Locate every Plasmodium falciparum-infected red blood cell.
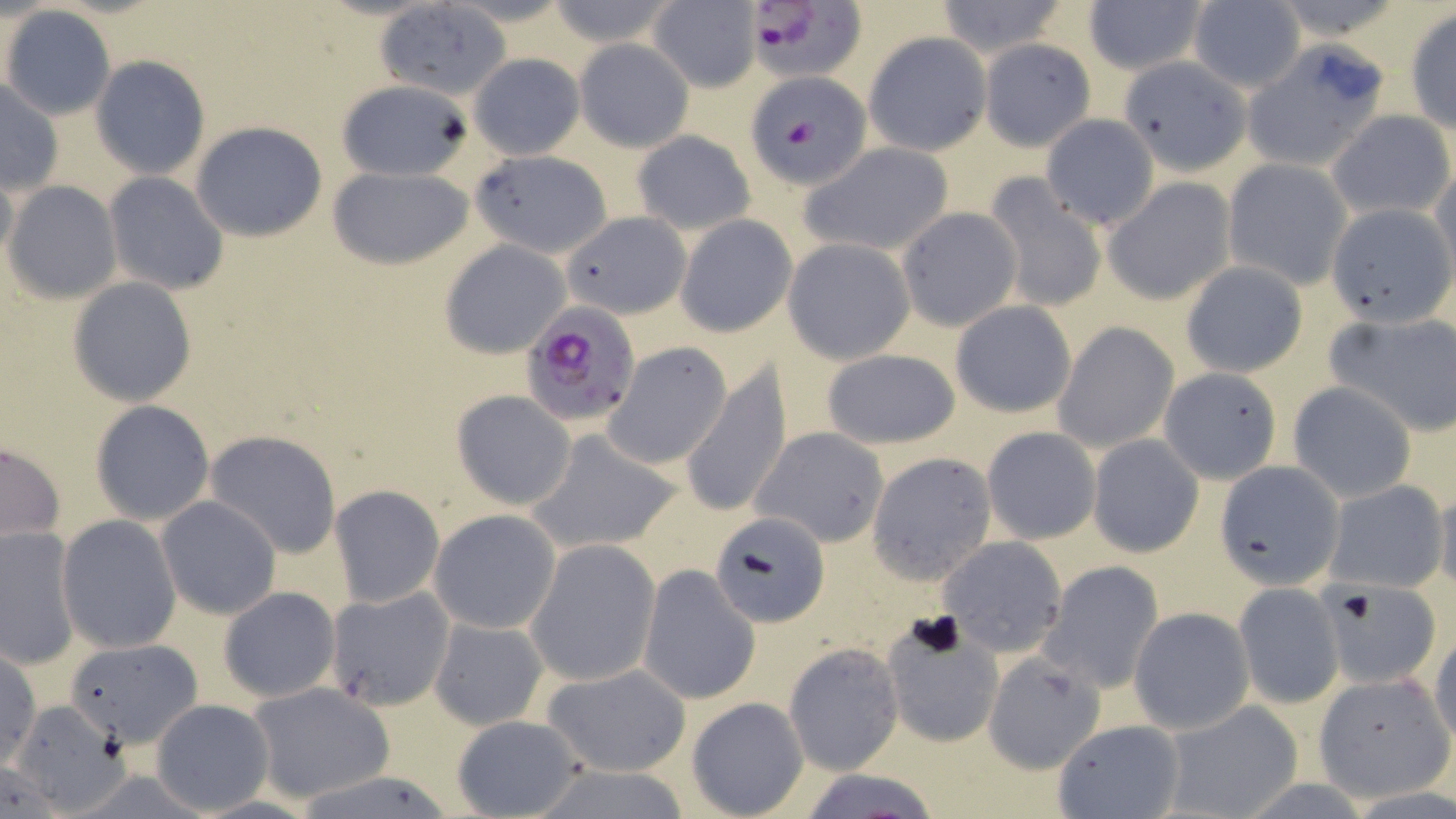
Approximate bounding boxes as [x1, y1, x2, y2] in pixels.
Plasmodium falciparum-infected red blood cells: [739, 3, 867, 83], [518, 299, 640, 426].

Uninfected red blood cell locations: [539, 0, 683, 50], [932, 0, 1073, 59], [648, 1, 761, 92], [1081, 2, 1210, 78], [1187, 2, 1306, 93], [378, 5, 509, 94], [1, 6, 118, 121], [1405, 10, 1455, 135], [864, 33, 990, 156], [978, 38, 1096, 149], [573, 39, 694, 151], [1242, 43, 1394, 172], [468, 52, 585, 159], [90, 55, 211, 179], [1120, 56, 1248, 174], [747, 68, 875, 192], [1, 79, 63, 196], [334, 79, 476, 181], [1328, 110, 1455, 222], [1040, 114, 1159, 230], [189, 121, 330, 241], [632, 130, 755, 235], [800, 142, 955, 257], [470, 151, 609, 255], [1222, 159, 1352, 288], [0, 163, 18, 272], [327, 164, 475, 270], [1430, 167, 1456, 283], [104, 172, 229, 294], [982, 174, 1107, 315], [1102, 178, 1237, 305], [4, 182, 121, 303], [1326, 201, 1455, 327], [897, 206, 1023, 331], [561, 209, 691, 320], [674, 214, 797, 338], [782, 238, 916, 364], [440, 239, 572, 357], [1179, 261, 1309, 379], [68, 276, 196, 405], [949, 301, 1078, 419], [1327, 311, 1456, 437], [1053, 321, 1178, 453], [604, 342, 731, 469], [818, 349, 962, 449], [681, 360, 792, 520], [1159, 368, 1282, 484], [1288, 382, 1416, 502], [450, 390, 577, 510], [89, 400, 215, 523], [980, 426, 1101, 544], [752, 427, 891, 548], [204, 429, 343, 559], [528, 429, 681, 557], [1088, 435, 1204, 558], [0, 439, 66, 547], [867, 452, 996, 583], [1215, 461, 1344, 590], [1324, 482, 1448, 593], [1430, 483, 1456, 595], [329, 485, 445, 609], [156, 495, 281, 620], [429, 509, 561, 634], [709, 510, 830, 627], [55, 515, 182, 653], [0, 526, 82, 670], [936, 536, 1068, 657], [525, 539, 660, 686], [1041, 561, 1164, 693], [639, 565, 760, 703], [1235, 584, 1343, 709], [1318, 584, 1440, 683], [324, 585, 455, 712], [217, 586, 341, 703], [1128, 607, 1254, 734], [428, 614, 549, 729], [880, 619, 1004, 748], [1429, 633, 1456, 746], [64, 636, 201, 747], [783, 643, 903, 775], [0, 647, 41, 770], [981, 651, 1107, 774], [540, 663, 692, 778], [1314, 674, 1454, 800], [245, 681, 396, 804], [687, 697, 809, 818], [150, 699, 273, 815], [6, 700, 131, 812], [1157, 702, 1304, 819], [448, 713, 586, 818], [1050, 719, 1185, 818], [791, 768, 946, 817]. Slide-level diagnosis: Plasmodium falciparum. Captured at 1000x magnification. Image is 1456×819 pixels. Single field of view. Optical microscopy. May-Grünwald-Giemsa-stained preparation. Thin blood smear.